Assess the morphology of the red blood cells.
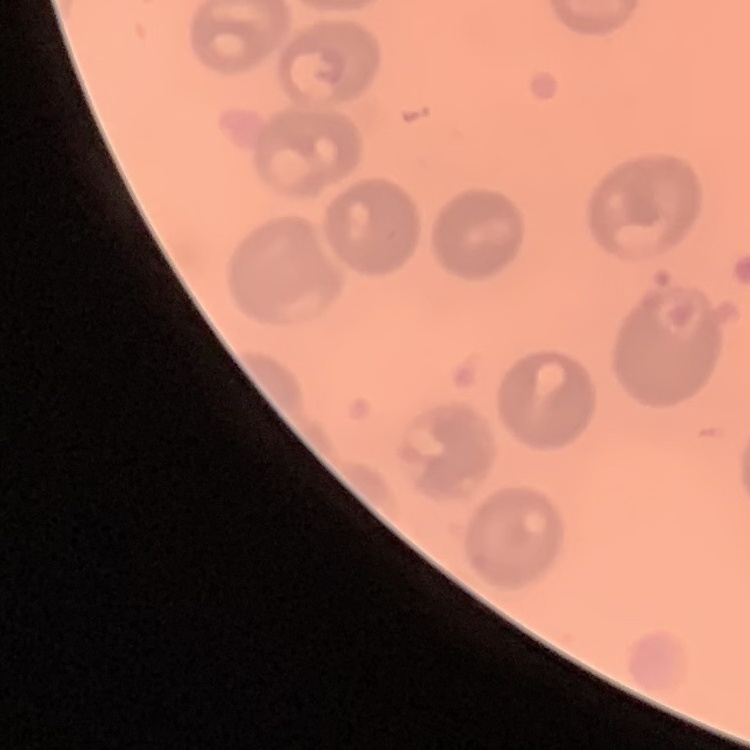

They show no rouleaux formation.

stain: Field's or Giemsa
image_type: one tile cut from a larger photomicrograph
preparation: thin peripheral smear